Outline each uninfected red blood cell.
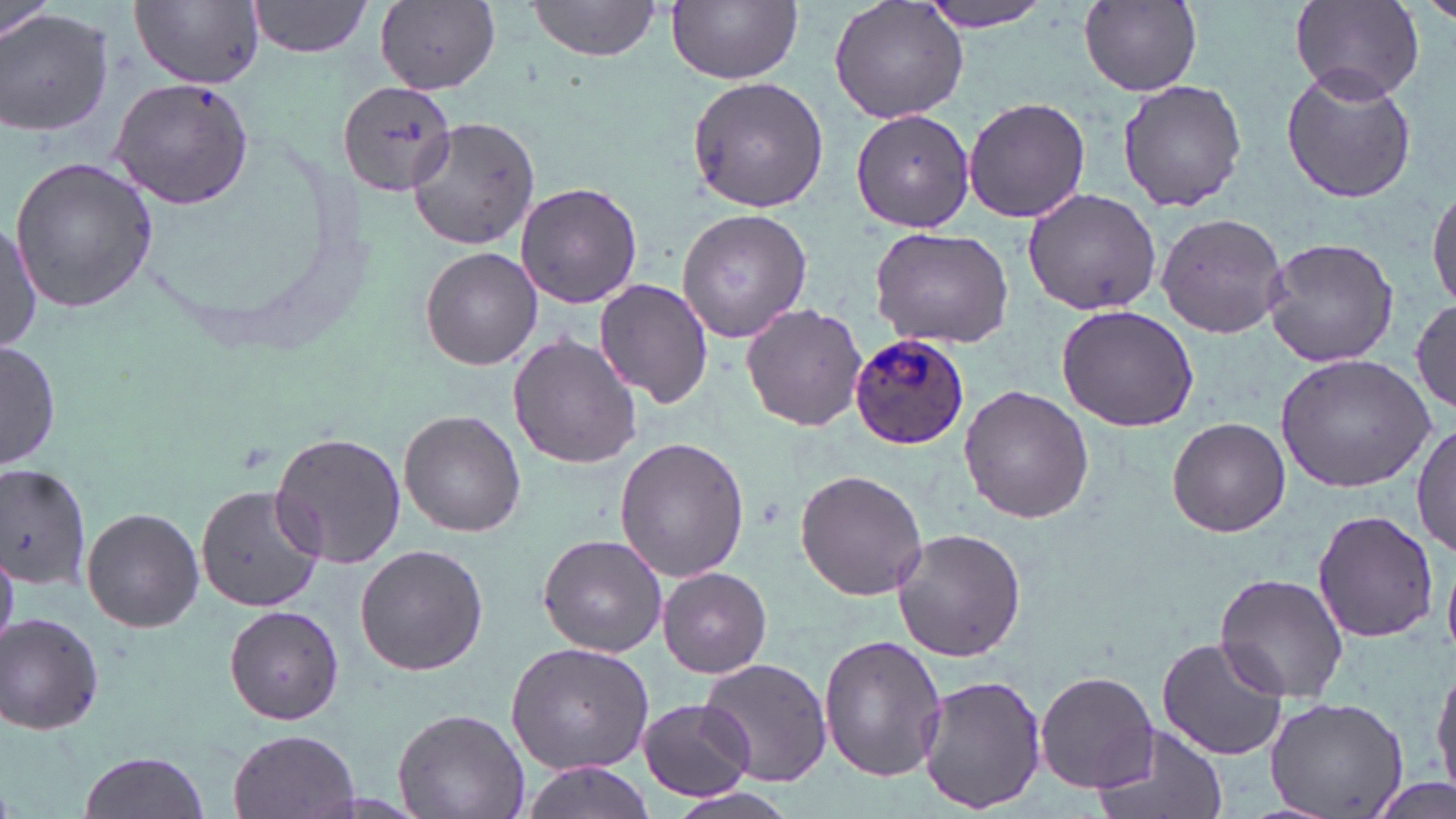
Approximate bounding boxes as (x1, y1, x2, y2) in pixels.
Uninfected red blood cells: (829, 0, 973, 125), (919, 0, 1060, 32), (1419, 0, 1455, 27), (247, 1, 374, 58), (525, 1, 662, 66), (668, 1, 802, 84), (1289, 1, 1424, 104), (2, 2, 55, 48), (133, 2, 265, 88), (1078, 2, 1202, 95), (376, 3, 501, 94), (0, 9, 114, 141), (1280, 66, 1417, 206), (685, 74, 828, 213), (109, 76, 254, 210), (1116, 77, 1247, 214), (337, 79, 459, 196), (962, 96, 1091, 223), (850, 107, 977, 232), (402, 116, 544, 252), (8, 157, 160, 313), (1429, 180, 1456, 313), (515, 182, 642, 309), (1019, 188, 1166, 316), (677, 208, 812, 343), (1155, 212, 1287, 337), (0, 220, 39, 355), (869, 227, 1015, 350), (1262, 236, 1400, 368), (420, 247, 542, 370), (594, 278, 713, 409), (1412, 298, 1455, 411), (740, 303, 868, 431), (1054, 305, 1200, 431), (508, 334, 642, 469), (1, 339, 62, 469), (1276, 354, 1436, 490), (959, 386, 1094, 524), (400, 411, 526, 536), (1166, 417, 1290, 537), (1412, 424, 1455, 558), (269, 431, 409, 568), (615, 438, 748, 582), (0, 463, 94, 591), (795, 468, 928, 600), (195, 485, 325, 612), (81, 506, 204, 632), (1310, 507, 1440, 645), (890, 528, 1026, 662), (537, 533, 667, 656), (355, 543, 489, 677), (656, 567, 773, 678), (1213, 572, 1351, 703), (224, 606, 344, 724), (1, 613, 105, 735), (817, 635, 949, 783), (1157, 636, 1288, 761), (507, 642, 656, 775), (697, 656, 833, 788), (1432, 657, 1456, 801), (1035, 670, 1159, 793), (916, 673, 1046, 816), (1265, 695, 1410, 819), (635, 697, 756, 802), (393, 706, 528, 819), (1091, 722, 1228, 819), (228, 729, 360, 818), (76, 749, 211, 819), (521, 761, 659, 819), (1365, 774, 1455, 819).

Plasmodium ovale-infected red blood cell locations: (849, 332, 969, 453). Slide-level diagnosis: Plasmodium ovale. May-Grünwald-Giemsa-stained preparation. Light microscopy. Image is 1456×819 pixels. Single field of view. Thin blood smear. 1000x magnification.